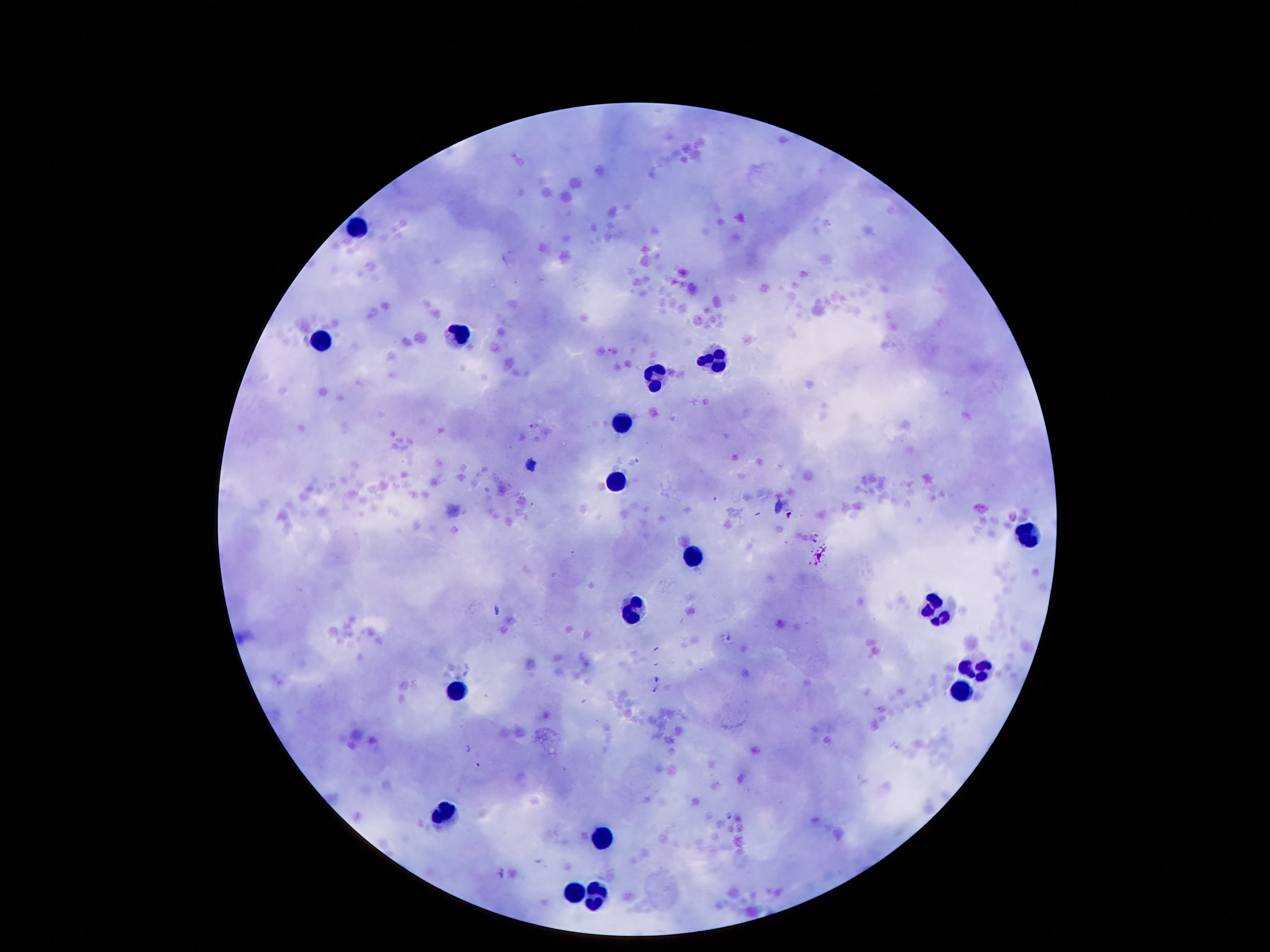
Approximate object centers, in pixels from the top-left corner. Leukocyte locations: (x=356, y=226), (x=319, y=342), (x=457, y=342), (x=715, y=362), (x=659, y=373), (x=623, y=420), (x=617, y=480), (x=1032, y=534), (x=692, y=558), (x=934, y=608), (x=634, y=610), (x=973, y=667), (x=957, y=691), (x=455, y=695), (x=444, y=806), (x=599, y=841), (x=575, y=892), (x=596, y=897). Photographed through the microscope eyepiece with a smartphone camera. Giemsa stain. Image is 1270×952 pixels. 100x magnification. Thick blood film. One field from this slide. Patient malaria status: not infected.